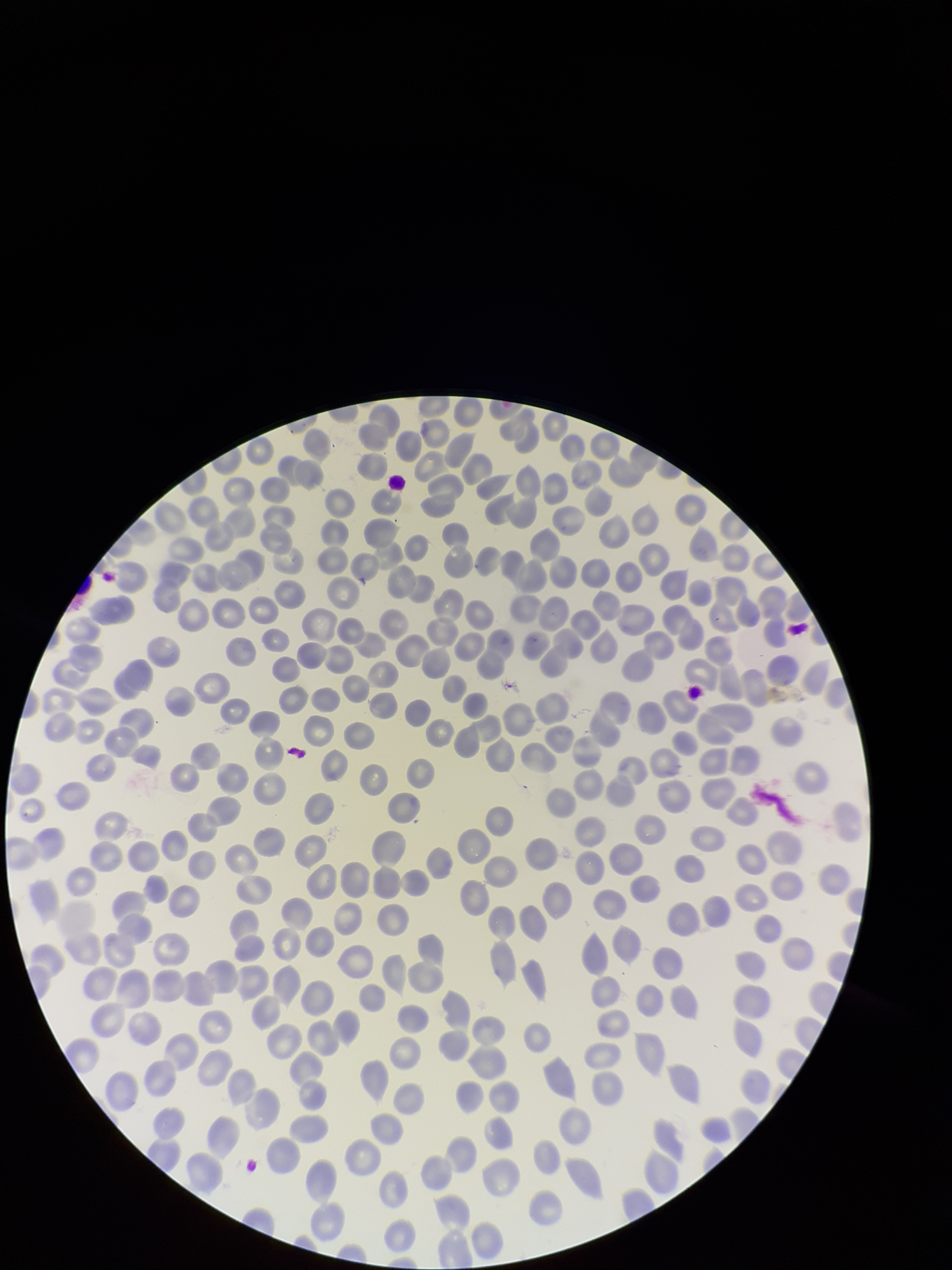
Parasitized red blood cell count: 0. Image is 952×1270 pixels. Stained with Giemsa. Patient malaria status: positive. Preparation: thin smear. Red blood cell count: 311. Parasitized red blood cells: none identified. One field from this slide. Photographed through the microscope eyepiece with a smartphone camera. Species reported for this patient: Plasmodium falciparum.